Assess the morphology of the erythrocytes.
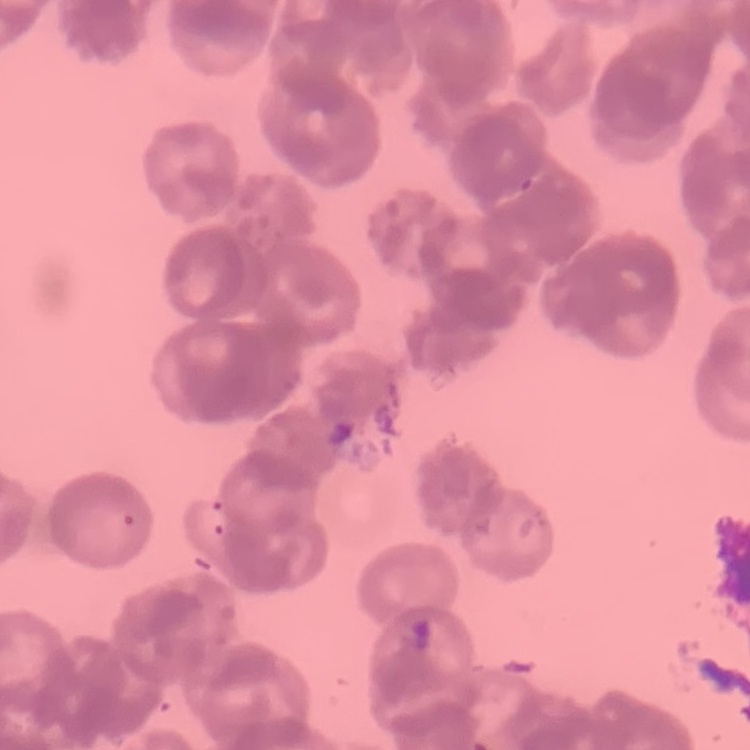

Rouleaux formation.

Thin peripheral smear. Square crop of a larger photomicrograph. Stained with either Field's or Giemsa.